Classify this cell by malaria status.
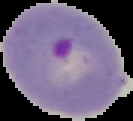

Parasitized.

image type = segmented cell region on a black background
preparation = thin blood smear
image size = 133×121 pixels